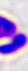

magnification: 400x
modality: micrograph
identification: leukocyte